Locate every malaria parasite.
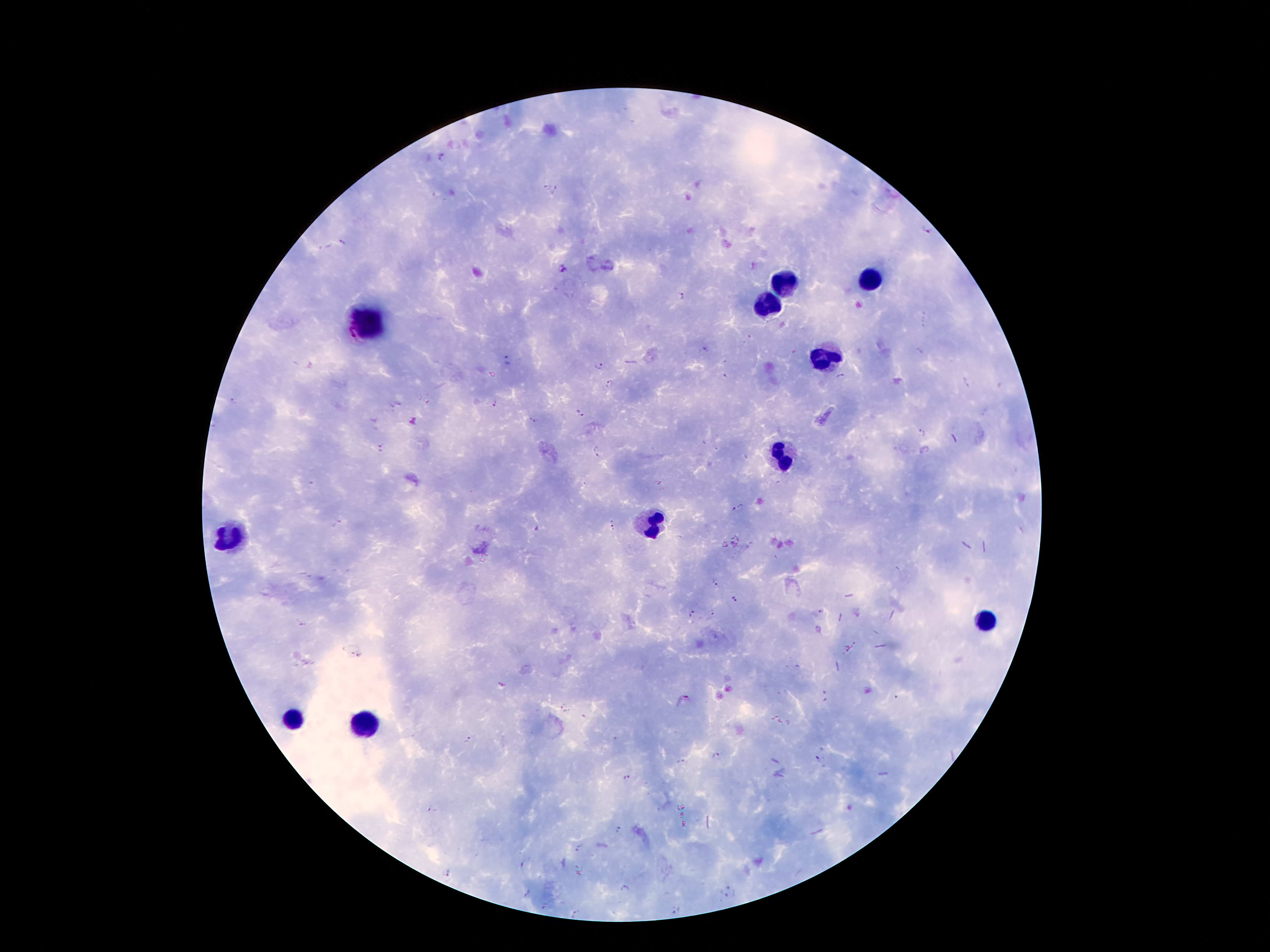
Approximate object centers, in pixels from the top-left corner.
Malaria parasites: (x=442, y=157), (x=546, y=186), (x=556, y=190), (x=924, y=230), (x=343, y=241), (x=325, y=247), (x=562, y=270), (x=682, y=297), (x=705, y=350), (x=918, y=350), (x=508, y=360), (x=598, y=365), (x=725, y=376), (x=840, y=377), (x=609, y=383), (x=968, y=383), (x=234, y=402), (x=398, y=403), (x=495, y=404), (x=391, y=405), (x=580, y=412), (x=412, y=421), (x=533, y=421), (x=922, y=434), (x=703, y=442), (x=382, y=447), (x=596, y=452), (x=778, y=483), (x=311, y=484), (x=737, y=507), (x=338, y=523), (x=614, y=526), (x=537, y=529), (x=680, y=537), (x=716, y=583), (x=734, y=599), (x=820, y=612), (x=693, y=613), (x=712, y=613), (x=302, y=625), (x=501, y=684), (x=825, y=691), (x=687, y=699), (x=825, y=700), (x=565, y=708), (x=466, y=740), (x=717, y=756), (x=820, y=760), (x=680, y=761), (x=627, y=777), (x=851, y=808), (x=432, y=809), (x=619, y=829), (x=577, y=848), (x=524, y=865), (x=449, y=873), (x=625, y=888), (x=727, y=892), (x=526, y=893), (x=675, y=911), (x=576, y=913).

leukocyte locations = (x=872, y=277), (x=788, y=282), (x=766, y=304), (x=371, y=319), (x=823, y=359), (x=786, y=455), (x=652, y=524), (x=232, y=534), (x=986, y=618), (x=289, y=719), (x=368, y=719)
capture = smartphone through the microscope eyepiece
stain = Giemsa
patient malaria status = infected with Plasmodium falciparum
magnification = 100x
field of view = single
image size = 1270×952 pixels
preparation = thick peripheral-blood smear